State the blood parasite species.
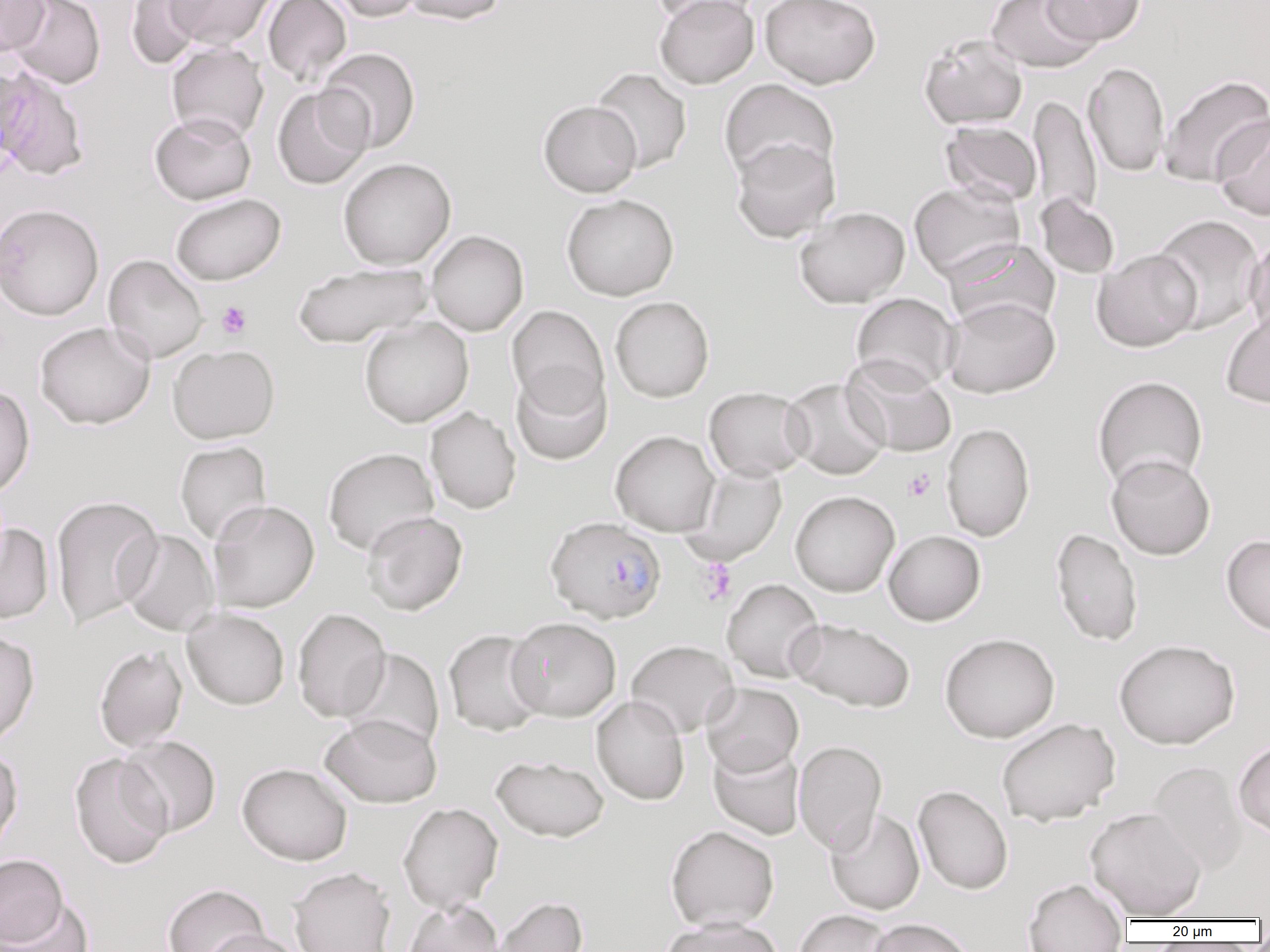

Plasmodium falciparum.

field_of_view: single
modality: light microscopy
image_size: 1270×952 pixels
preparation: thin blood film
uninfected_red_blood_cell_locations: 'approximate bounding boxes as [x1, y1, x2, y2] in pixels: [0, 0, 49, 56], [6, 0, 105, 89], [124, 0, 210, 70], [167, 0, 275, 49], [262, 0, 352, 85], [322, 0, 426, 22], [399, 0, 507, 25], [650, 0, 762, 26], [654, 0, 759, 89], [760, 0, 881, 89], [986, 0, 1101, 73], [1042, 0, 1145, 45], [919, 33, 1028, 130], [166, 42, 269, 143], [317, 48, 420, 153], [1083, 62, 1169, 177], [0, 63, 36, 174], [0, 67, 87, 180], [591, 67, 692, 173], [1159, 74, 1269, 188], [719, 79, 839, 184], [272, 86, 373, 190], [1028, 94, 1102, 224], [538, 100, 642, 197], [149, 112, 256, 205], [1213, 114, 1270, 221], [940, 120, 1042, 206], [731, 137, 840, 242], [337, 158, 456, 270], [909, 181, 1025, 282], [170, 193, 285, 286], [1036, 193, 1120, 279], [562, 194, 679, 300], [0, 203, 104, 320], [794, 206, 910, 308], [1150, 214, 1265, 333], [427, 230, 529, 336], [1244, 235, 1270, 342], [945, 238, 1059, 331], [1092, 249, 1202, 351], [103, 255, 208, 363], [292, 262, 433, 348], [851, 293, 960, 392], [610, 296, 714, 402], [942, 296, 1060, 398], [507, 305, 609, 415], [1221, 310, 1270, 409], [359, 317, 474, 427], [34, 321, 156, 430], [167, 344, 280, 443], [841, 355, 957, 457], [511, 364, 612, 466], [1092, 375, 1208, 492], [781, 378, 890, 480], [0, 384, 34, 499], [703, 387, 811, 480], [425, 406, 521, 514], [941, 422, 1035, 541], [610, 430, 720, 536], [175, 440, 272, 545], [323, 447, 439, 556], [1106, 454, 1215, 560], [684, 463, 787, 565], [790, 491, 899, 596], [49, 495, 164, 629], [207, 500, 319, 613], [361, 510, 468, 615], [0, 521, 54, 624], [1050, 527, 1143, 647], [118, 528, 220, 636], [884, 530, 986, 625], [1221, 534, 1270, 636], [721, 578, 824, 683], [182, 607, 290, 710], [292, 608, 391, 723], [506, 617, 621, 721], [789, 618, 915, 712], [443, 629, 548, 736], [0, 630, 39, 747], [939, 633, 1060, 743], [1114, 639, 1240, 749], [626, 640, 738, 737], [94, 645, 188, 751], [341, 648, 444, 753], [700, 682, 803, 776], [591, 695, 690, 805], [320, 713, 442, 808], [995, 718, 1121, 826], [119, 736, 221, 837], [1233, 739, 1270, 838], [793, 740, 887, 854], [708, 741, 805, 840], [0, 745, 23, 857], [69, 752, 173, 870], [491, 755, 609, 842], [237, 762, 353, 866], [1149, 762, 1247, 876], [913, 785, 1013, 895], [398, 802, 503, 914], [1085, 806, 1207, 920], [825, 808, 925, 915], [665, 825, 779, 931], [0, 854, 69, 948], [288, 866, 398, 952], [1023, 879, 1128, 952], [162, 883, 270, 952], [491, 895, 588, 952], [2, 897, 92, 952], [401, 900, 505, 952], [793, 909, 893, 952], [659, 917, 785, 952], [868, 918, 976, 952], [201, 929, 306, 952]'
platelet_locations: 'approximate bounding boxes as [x1, y1, x2, y2] in pixels: [216, 301, 252, 339], [903, 469, 936, 501], [697, 558, 736, 605]'
plasmodium_falciparum_infected_red_blood_cell_locations: 'approximate bounding boxes as [x1, y1, x2, y2] in pixels: [545, 517, 666, 623]'
magnification: 1000x